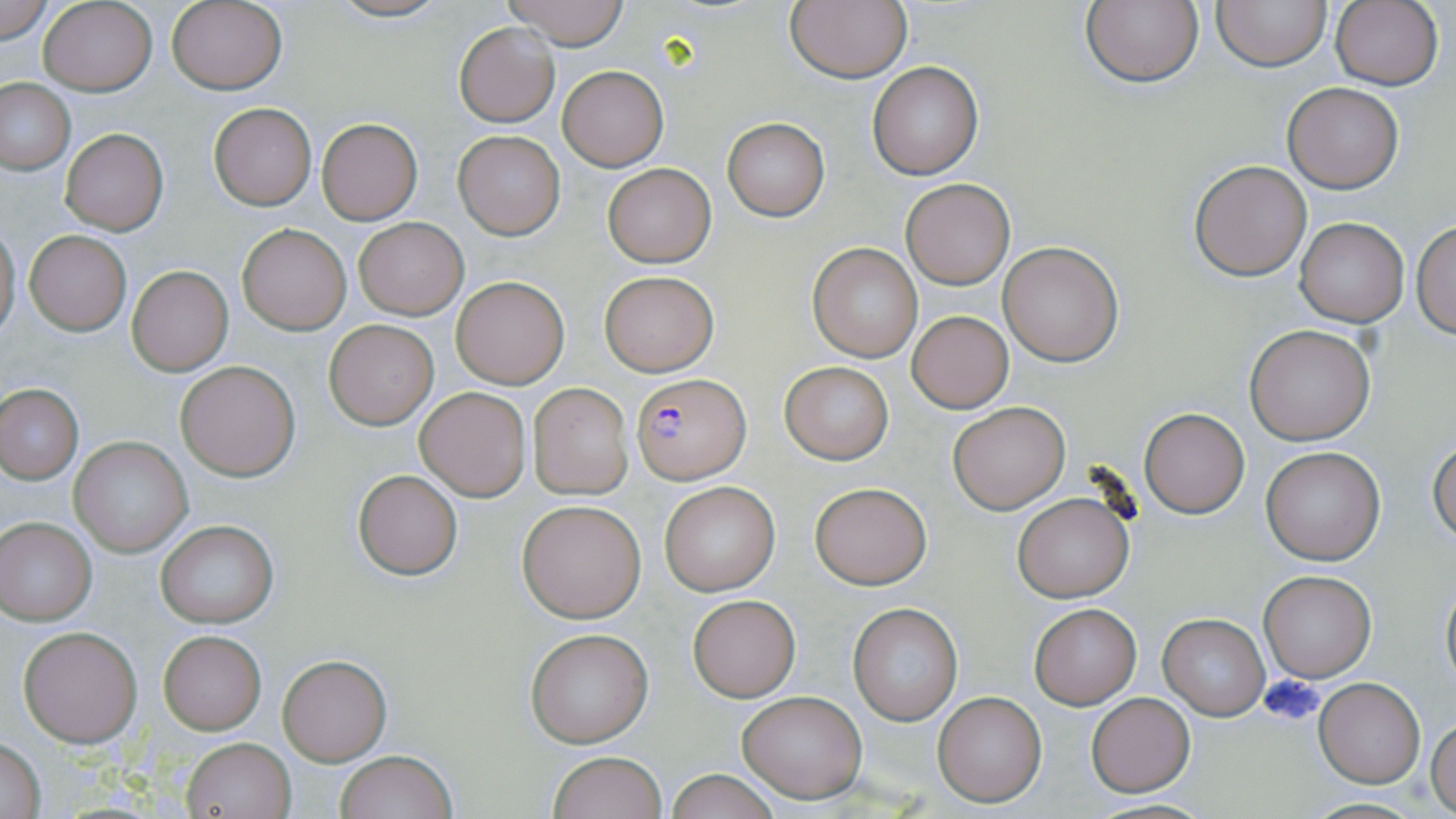

Approximate bounding boxes as (x1,y1)-(x2,y2) corner pairs in pixels. Plasmodium falciparum-infected red blood cell locations: (633,373)-(750,484). Uninfected red blood cell locations: (324,0)-(454,22), (500,0)-(632,48), (1212,0)-(1331,71), (1332,0)-(1443,90), (38,1)-(156,94), (166,1)-(287,94), (1080,1)-(1203,88), (0,2)-(54,45), (783,2)-(911,83), (453,21)-(561,128), (868,62)-(982,178), (557,65)-(669,170), (0,79)-(75,175), (1283,83)-(1402,193), (208,103)-(316,210), (316,118)-(423,224), (722,118)-(830,220), (62,129)-(167,235), (452,131)-(565,240), (1189,160)-(1311,280), (603,163)-(715,266), (899,176)-(1015,290), (1295,216)-(1409,327), (353,217)-(468,319), (1413,218)-(1456,338), (0,223)-(21,340), (237,223)-(351,334), (25,231)-(131,336), (997,241)-(1125,367), (808,242)-(925,364), (127,266)-(233,376), (600,271)-(718,376), (451,276)-(570,389), (907,310)-(1014,413), (324,319)-(438,428), (1245,324)-(1376,445), (175,360)-(301,481), (780,362)-(893,463), (527,383)-(633,499), (0,384)-(84,483), (415,387)-(531,501), (947,400)-(1071,515), (1140,407)-(1251,519), (69,436)-(192,556), (1428,438)-(1455,545), (1260,446)-(1384,565), (351,469)-(463,580), (660,481)-(781,596), (810,482)-(931,589), (1012,494)-(1134,603), (518,498)-(647,622), (0,517)-(97,624), (155,520)-(278,627), (1258,570)-(1377,682), (1440,574)-(1455,689), (688,594)-(800,702), (847,603)-(963,726), (1028,603)-(1142,709), (1159,613)-(1269,719), (18,625)-(142,747), (524,627)-(653,748), (158,630)-(266,734), (277,652)-(392,765), (1315,678)-(1424,787), (737,689)-(867,803), (931,689)-(1048,807), (1086,693)-(1196,796), (1427,717)-(1456,816), (182,736)-(294,818), (0,738)-(47,818), (334,750)-(457,819), (546,751)-(666,819), (663,770)-(787,819). Slide-level diagnosis: Plasmodium falciparum. Captured at 1000x magnification. May-Grünwald-Giemsa-stained preparation. One field of a larger specimen. Image is 1456×819 pixels. Thin blood film. Light microscopy.